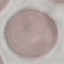 Result: no malaria parasites seen. Automatically extracted cell patch, resized to 64 × 64 pixels. Giemsa-stained preparation. Thin blood film. Acquired by smartphone through the microscope eyepiece.